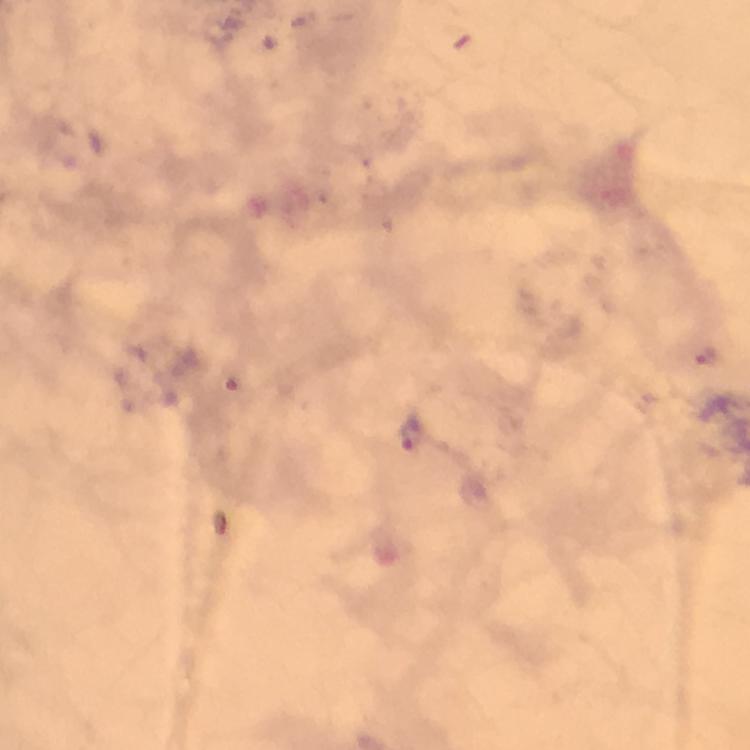

Approximate centers as (x, y) in pixels.
Summary:
  - Malaria parasite locations: (706, 358), (414, 433)
  - Capture: smartphone camera through the microscope
  - Context: from a malaria diagnostic workup
  - Preparation: thick smear
  - Magnification: 100x
  - Cropped from: a single field of view
  - Image size: 750×750 pixels
  - Immersion oil: applied
  - Stain: Giemsa